State which parasite is depicted.
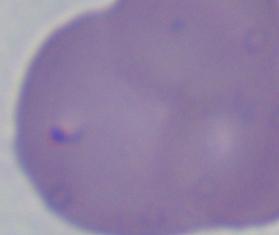

This is Babesia.

Photomicrograph. Captured at 1000x magnification.